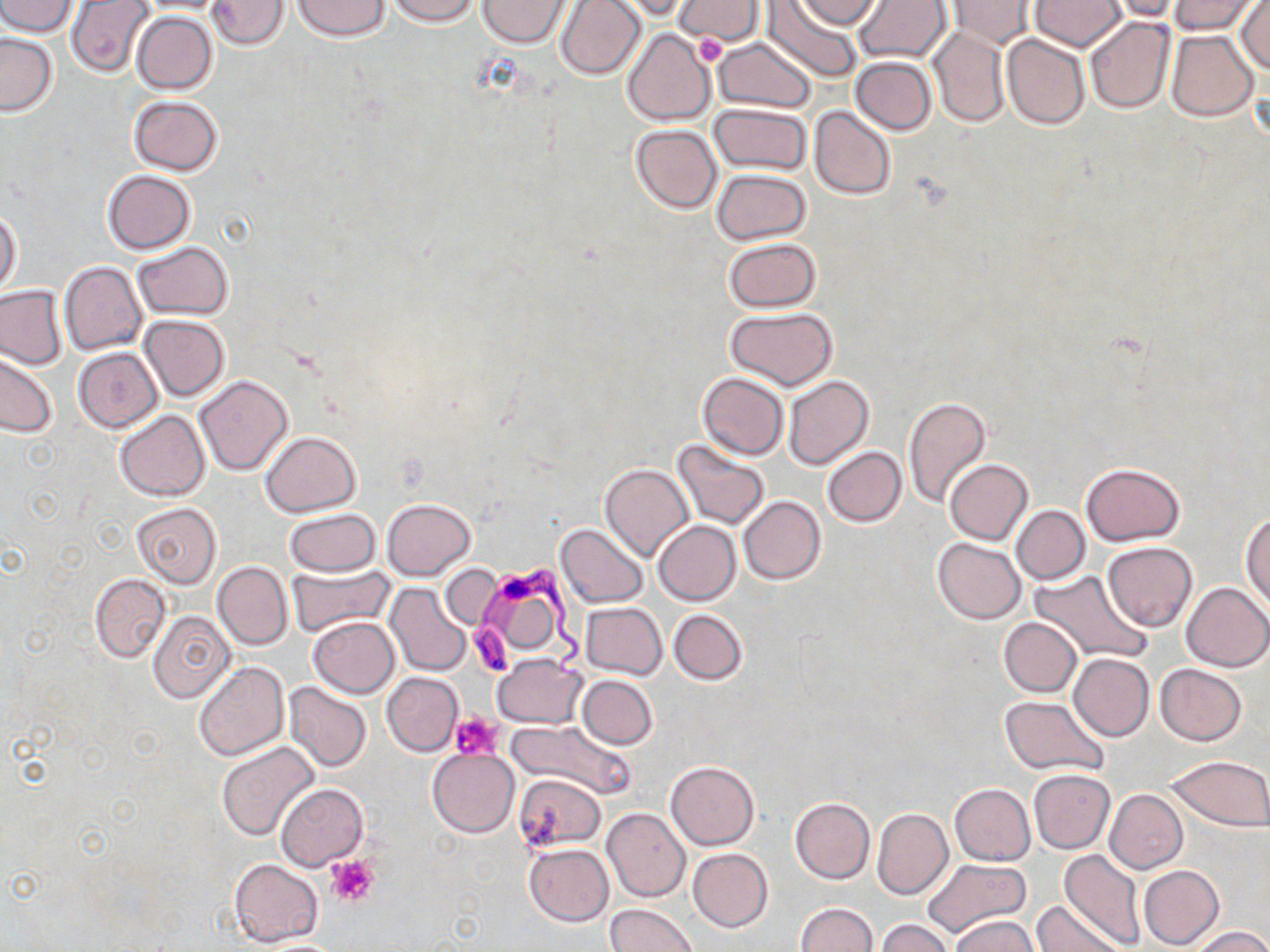

{
  "slide_level_diagnosis": "Trypanosoma brucei",
  "modality": "optical microscopy",
  "field_of_view": "single",
  "stain": "May-Grünwald-Giemsa",
  "preparation": "thin blood film",
  "uninfected_red_blood_cell_locations": "approximate bounding boxes as (x1,y1)-(x2,y2) corner pairs in pixels: (0,0)-(78,37), (67,0)-(156,77), (137,0)-(232,14), (208,0)-(287,49), (292,0)-(389,41), (386,0)-(481,25), (478,0)-(572,48), (555,0)-(646,81), (609,0)-(694,22), (673,0)-(766,45), (765,0)-(864,82), (793,0)-(884,31), (853,0)-(952,64), (1029,0)-(1126,51), (1102,0)-(1186,21), (1167,0)-(1262,35), (1234,0)-(1270,74), (947,1)-(1039,50), (132,11)-(218,95), (1084,16)-(1176,116), (927,25)-(1009,128), (622,29)-(716,126), (1166,29)-(1259,121), (1,32)-(58,116), (1002,34)-(1091,129), (713,36)-(818,115), (851,56)-(936,134), (128,95)-(223,175), (710,103)-(812,175), (810,106)-(895,201), (630,124)-(721,213), (712,168)-(810,245), (101,170)-(195,254), (1,208)-(22,295), (722,238)-(822,312), (133,242)-(234,320), (59,262)-(147,354), (0,285)-(67,369), (725,306)-(837,389), (138,314)-(230,400), (72,348)-(163,433), (0,352)-(57,438), (697,372)-(789,460), (194,374)-(294,475), (783,375)-(874,471), (902,396)-(992,509), (115,410)-(209,501), (260,431)-(360,515), (672,439)-(770,529), (821,447)-(906,526), (945,459)-(1033,545), (599,462)-(694,562), (1082,462)-(1183,545), (739,495)-(826,584), (382,498)-(475,580), (130,502)-(223,587), (1011,505)-(1089,584), (284,509)-(379,577), (1242,514)-(1270,611), (653,521)-(741,605), (555,524)-(648,608), (933,538)-(1025,624), (1102,541)-(1197,631), (212,561)-(292,651), (286,565)-(395,637), (439,565)-(504,630), (1030,571)-(1148,664), (90,574)-(169,661), (1180,582)-(1270,672), (386,584)-(474,677), (581,602)-(668,679), (669,609)-(747,684), (148,610)-(236,703), (308,617)-(400,698), (998,617)-(1082,697), (1069,653)-(1154,741), (492,654)-(586,728), (194,661)-(290,760), (1155,663)-(1247,746), (381,672)-(463,756), (577,674)-(657,749), (284,683)-(372,772), (999,695)-(1109,776), (507,719)-(635,798), (216,742)-(319,840), (428,748)-(518,836), (1167,755)-(1270,831), (664,761)-(759,850), (1028,769)-(1116,853), (514,772)-(605,852), (276,783)-(368,871), (949,784)-(1034,865), (1105,789)-(1188,873), (789,796)-(875,883), (602,808)-(689,901), (872,808)-(953,899), (524,844)-(613,926), (688,848)-(772,931), (1059,849)-(1145,949), (921,857)-(1032,941), (228,860)-(322,946), (1138,865)-(1224,950), (1032,900)-(1124,952), (794,903)-(876,952), (604,904)-(698,952), (949,914)-(1040,952), (876,919)-(954,952), (1190,926)-(1270,952)",
  "magnification": "1000x",
  "platelet_locations": "approximate bounding boxes as (x1,y1)-(x2,y2) corner pairs in pixels: (694,34)-(727,66), (451,712)-(504,760), (326,855)-(378,907)",
  "trypanosoma_brucei_locations": "approximate bounding boxes as (x1,y1)-(x2,y2) corner pairs in pixels: (467,559)-(590,684)",
  "image_size": "1270×952 pixels"
}